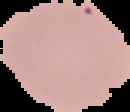

Result: no Plasmodium parasites detected. Image is 130×112 pixels. From a thin blood film. Segmented cell region on a black background.